Outline white blood cells.
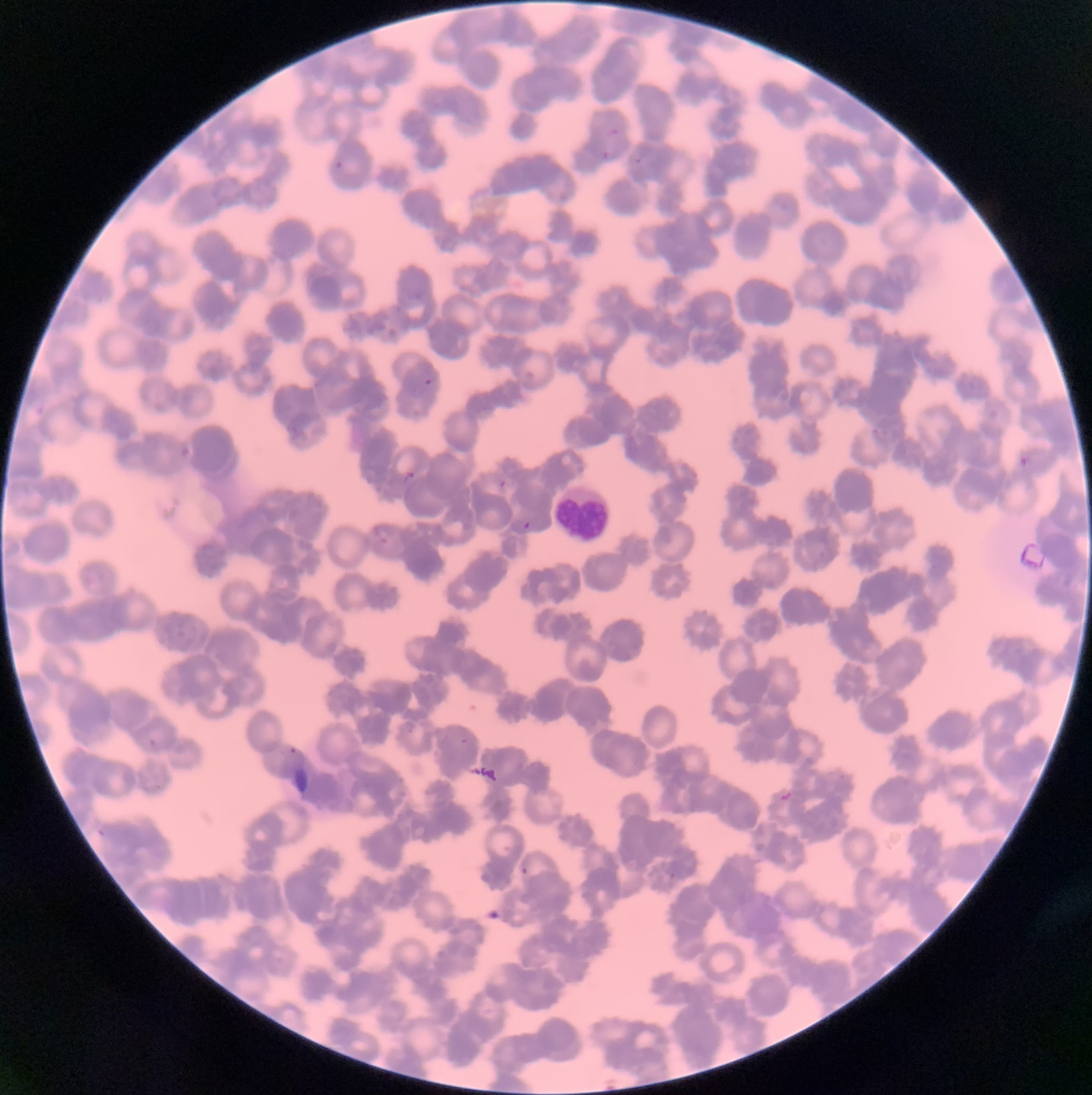

Approximate bounding boxes as [x1, y1, x2, y2] in pixels.
White blood cells: [554, 484, 610, 541].

Plasmodium parasite locations: [607, 126, 619, 137], [602, 150, 611, 160], [635, 157, 642, 166], [334, 160, 345, 170], [424, 378, 434, 386], [1018, 455, 1028, 468], [403, 470, 415, 484], [498, 478, 507, 489], [522, 521, 531, 530], [374, 526, 391, 544], [460, 737, 469, 745], [286, 747, 306, 770], [521, 867, 528, 877]. The red blood cells show rouleaux formation. Image is 1092×1095 pixels. Light microscopy. Thin blood film.